Locate every uninfected red blood cell.
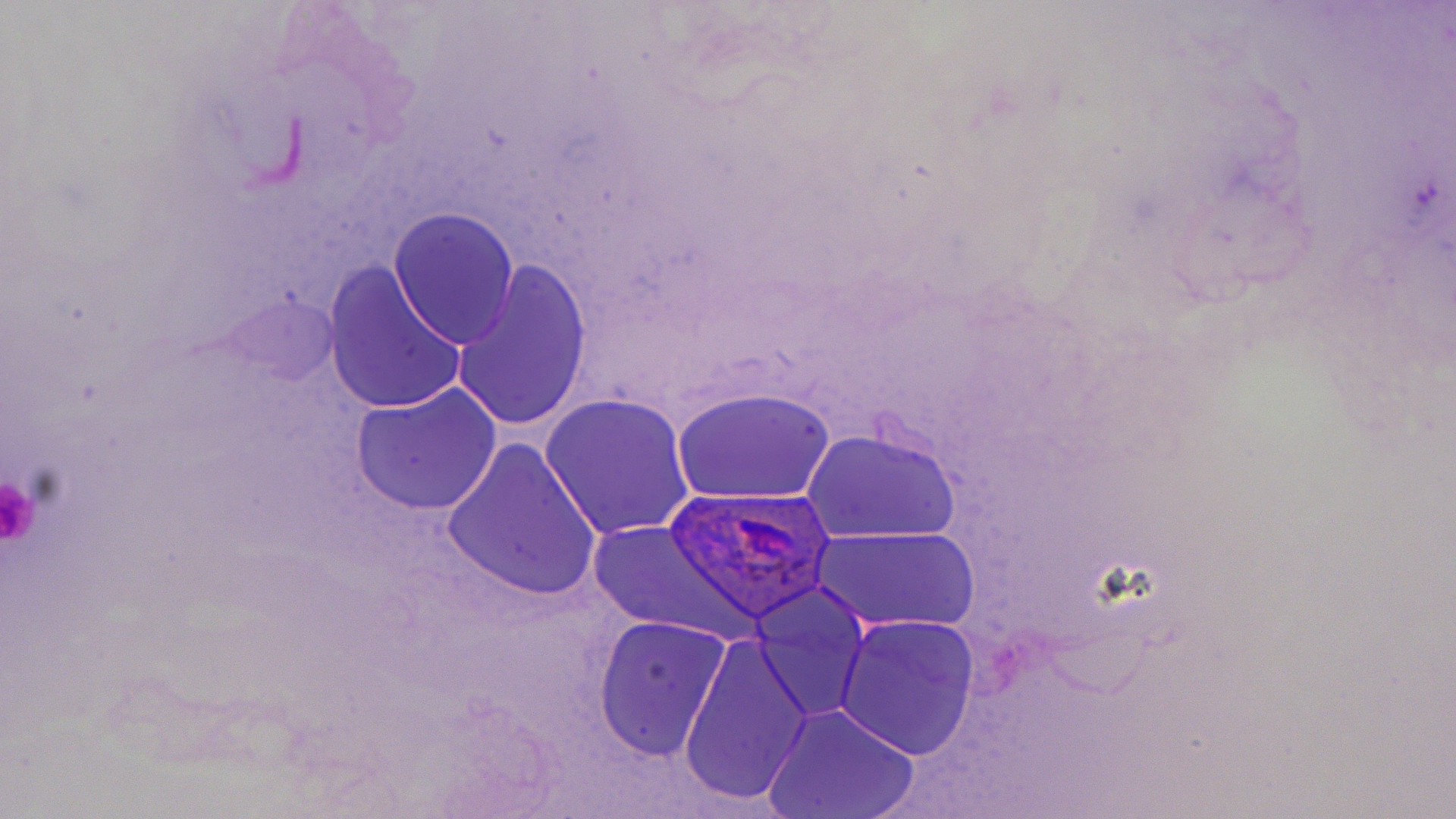
Approximate bounding boxes as (x1,y1)-(x2,y2) corner pairs in pixels.
Uninfected red blood cells: (388,208)-(519,348), (451,262)-(592,435), (324,266)-(466,416), (350,384)-(503,516), (671,386)-(836,508), (540,393)-(698,543), (804,430)-(962,546), (441,441)-(600,603), (586,518)-(764,643), (812,525)-(981,636), (751,583)-(870,723), (834,615)-(981,760), (594,618)-(732,761), (679,636)-(814,807), (764,704)-(920,819).

Summary:
  - Plasmodium ovale-infected red blood cell locations: (660,486)-(839,622)
  - Platelet locations: (0,473)-(41,547)
  - Slide-level diagnosis: Plasmodium ovale
  - Preparation: thin blood film
  - Stain: May-Grünwald-Giemsa
  - Modality: light microscopy
  - Field of view: single
  - Magnification: 1000x
  - Image size: 1456×819 pixels